Name the parasite shown.
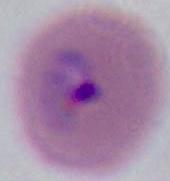
Plasmodium.

Captured at either 400x or 1000x magnification. Photomicrograph.